Outline each blood parasite and name the species.
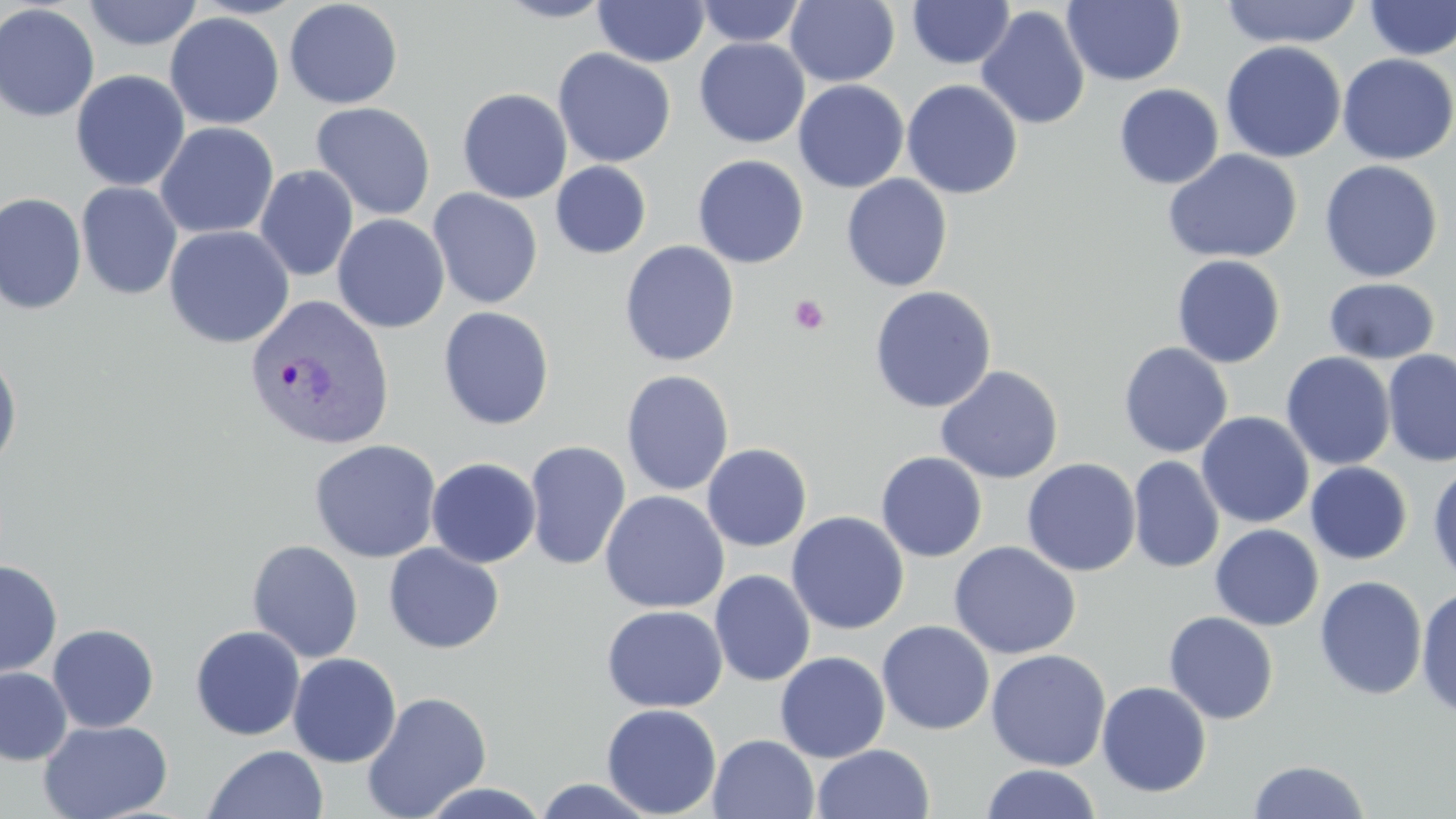

Approximate bounding boxes as named x1/y1/x2/y2 corners in pixels.
Plasmodium vivax-infected red blood cells: (x1=244, y1=294, x2=395, y2=451).
No Plasmodium falciparum, Plasmodium ovale, Plasmodium malariae, Babesia divergens, or Trypanosoma brucei observed.

Summary:
  - Uninfected red blood cell locations: (x1=81, y1=0, x2=204, y2=51), (x1=283, y1=0, x2=403, y2=109), (x1=493, y1=0, x2=614, y2=23), (x1=907, y1=0, x2=1015, y2=69), (x1=1063, y1=0, x2=1186, y2=86), (x1=1219, y1=0, x2=1363, y2=48), (x1=593, y1=1, x2=710, y2=67), (x1=695, y1=1, x2=806, y2=47), (x1=785, y1=1, x2=900, y2=87), (x1=1363, y1=1, x2=1456, y2=60), (x1=0, y1=3, x2=100, y2=122), (x1=976, y1=5, x2=1090, y2=130), (x1=164, y1=11, x2=285, y2=130), (x1=695, y1=38, x2=809, y2=148), (x1=1220, y1=41, x2=1346, y2=163), (x1=553, y1=48, x2=676, y2=168), (x1=1337, y1=53, x2=1455, y2=165), (x1=70, y1=69, x2=191, y2=191), (x1=793, y1=79, x2=909, y2=193), (x1=901, y1=79, x2=1023, y2=200), (x1=1114, y1=83, x2=1224, y2=189), (x1=457, y1=88, x2=572, y2=204), (x1=311, y1=102, x2=436, y2=221), (x1=155, y1=121, x2=279, y2=239), (x1=1163, y1=149, x2=1303, y2=264), (x1=692, y1=155, x2=809, y2=268), (x1=1319, y1=160, x2=1443, y2=283), (x1=550, y1=161, x2=652, y2=259), (x1=254, y1=164, x2=359, y2=281), (x1=841, y1=174, x2=952, y2=291), (x1=76, y1=181, x2=183, y2=301), (x1=427, y1=188, x2=543, y2=309), (x1=0, y1=192, x2=86, y2=315), (x1=332, y1=213, x2=450, y2=333), (x1=164, y1=224, x2=295, y2=349), (x1=619, y1=240, x2=740, y2=367), (x1=1171, y1=254, x2=1286, y2=368), (x1=1323, y1=278, x2=1440, y2=364), (x1=869, y1=285, x2=997, y2=413), (x1=438, y1=306, x2=555, y2=431), (x1=1118, y1=342, x2=1233, y2=458), (x1=0, y1=346, x2=23, y2=473), (x1=1381, y1=349, x2=1456, y2=466), (x1=1280, y1=352, x2=1396, y2=470), (x1=935, y1=365, x2=1064, y2=484), (x1=621, y1=369, x2=735, y2=496), (x1=1196, y1=412, x2=1314, y2=528), (x1=309, y1=439, x2=442, y2=563), (x1=524, y1=440, x2=632, y2=571), (x1=702, y1=443, x2=812, y2=551), (x1=876, y1=452, x2=988, y2=563), (x1=1128, y1=456, x2=1225, y2=574), (x1=426, y1=457, x2=541, y2=568), (x1=1021, y1=458, x2=1141, y2=577), (x1=1428, y1=461, x2=1456, y2=587), (x1=1305, y1=462, x2=1413, y2=565), (x1=599, y1=490, x2=729, y2=613), (x1=786, y1=512, x2=909, y2=635), (x1=1210, y1=524, x2=1323, y2=631), (x1=247, y1=540, x2=364, y2=663), (x1=947, y1=541, x2=1082, y2=660), (x1=383, y1=543, x2=505, y2=654), (x1=0, y1=560, x2=62, y2=679), (x1=710, y1=569, x2=815, y2=687), (x1=1314, y1=575, x2=1428, y2=701), (x1=1415, y1=585, x2=1456, y2=719), (x1=601, y1=605, x2=727, y2=712), (x1=1164, y1=611, x2=1279, y2=724), (x1=877, y1=620, x2=995, y2=735), (x1=47, y1=624, x2=159, y2=732), (x1=190, y1=625, x2=305, y2=741), (x1=985, y1=649, x2=1111, y2=771), (x1=774, y1=651, x2=890, y2=762), (x1=287, y1=653, x2=402, y2=768), (x1=0, y1=667, x2=72, y2=766), (x1=1096, y1=681, x2=1212, y2=797), (x1=361, y1=691, x2=492, y2=819), (x1=601, y1=703, x2=722, y2=818), (x1=38, y1=719, x2=173, y2=819), (x1=707, y1=734, x2=820, y2=819), (x1=812, y1=744, x2=935, y2=819), (x1=203, y1=745, x2=329, y2=819), (x1=1247, y1=759, x2=1371, y2=819), (x1=981, y1=764, x2=1103, y2=819), (x1=529, y1=778, x2=663, y2=818), (x1=415, y1=782, x2=553, y2=818)
  - Platelet locations: (x1=789, y1=294, x2=830, y2=335)
  - Slide-level diagnosis: Plasmodium vivax
  - Magnification: 1000x
  - Field of view: single
  - Image size: 1456×819 pixels
  - Preparation: thin blood film
  - Modality: optical microscopy
  - Stain: May-Grünwald-Giemsa